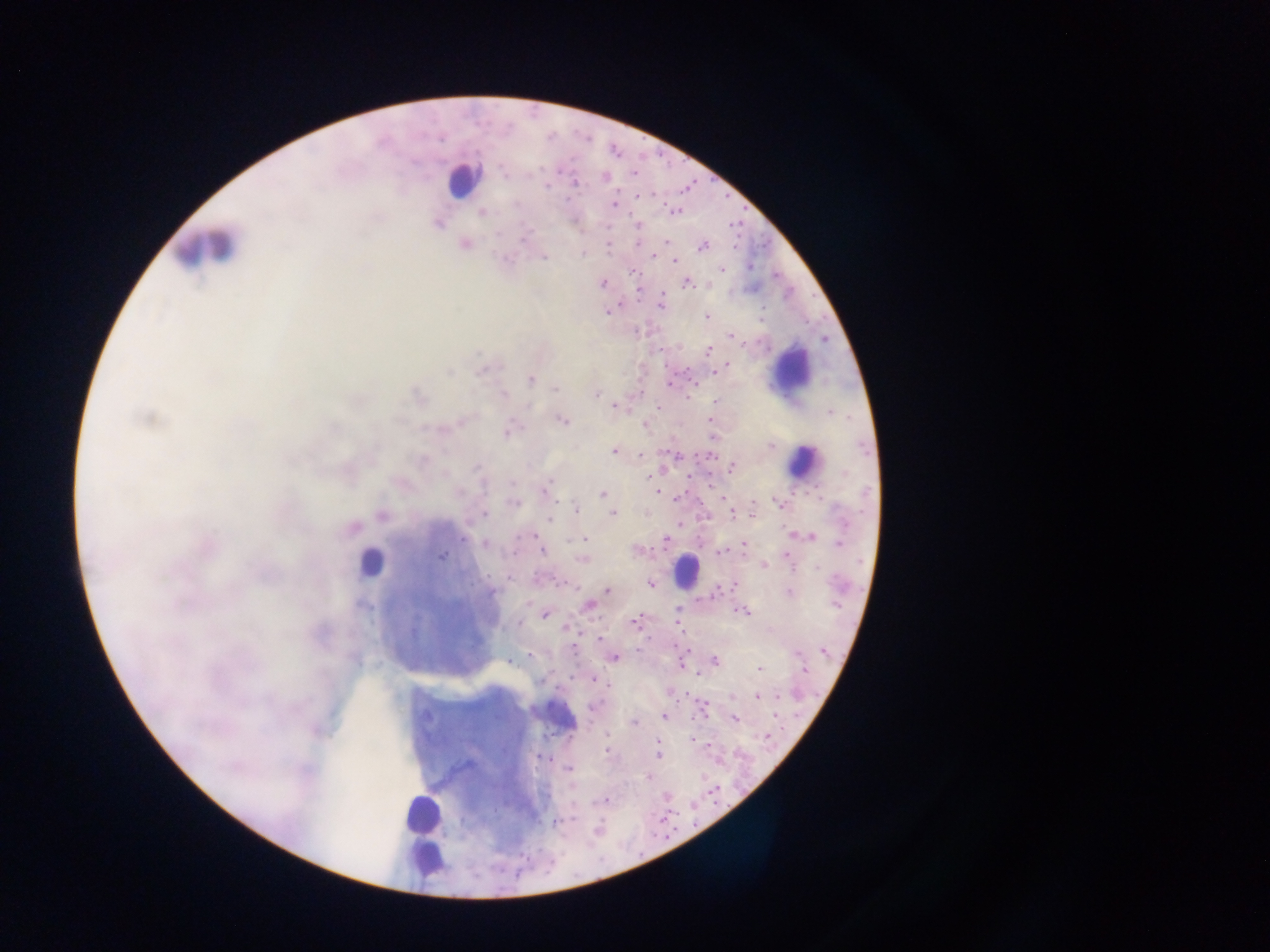

preparation = thick blood film
country = Ghana
image size = 1270×952 pixels
malaria parasite locations = approximate centers as {x, y} in pixels: {503, 174}, {529, 175}, {606, 177}, {575, 183}, {547, 186}, {638, 196}, {567, 200}, {614, 204}, {482, 212}, {438, 224}, {522, 239}, {638, 243}, {464, 244}, {702, 247}, {583, 253}, {653, 256}, {544, 257}, {674, 260}, {750, 266}, {721, 269}, {633, 272}, {603, 283}, {687, 283}, {662, 302}, {606, 312}, {707, 317}, {761, 319}, {732, 337}, {708, 349}, {480, 371}, {449, 372}, {715, 372}, {530, 379}, {670, 383}, {555, 388}, {596, 394}, {504, 395}, {689, 396}, {715, 402}, {615, 407}, {658, 407}, {830, 413}, {148, 418}, {562, 420}, {646, 426}, {507, 432}, {713, 436}, {771, 445}, {862, 448}, {613, 451}, {641, 455}, {678, 455}, {423, 460}, {476, 468}, {732, 469}, {514, 484}, {545, 491}, {655, 492}, {603, 493}, {514, 502}, {777, 502}, {753, 505}, {576, 508}, {732, 513}, {484, 514}, {612, 514}, {840, 514}, {381, 515}, {549, 519}, {351, 529}, {533, 536}, {812, 537}, {463, 539}, {584, 539}, {665, 541}, {485, 543}, {840, 544}, {744, 546}, {637, 550}, {543, 552}, {720, 554}, {441, 556}, {786, 556}, {581, 559}, {764, 565}, {791, 565}, {816, 568}, {510, 578}, {651, 583}, {734, 585}, {607, 590}, {790, 592}, {492, 593}, {835, 603}, {589, 606}, {677, 610}, {744, 611}, {544, 614}, {636, 621}, {520, 623}, {566, 627}, {600, 639}, {824, 651}, {798, 653}, {529, 655}, {614, 657}, {715, 660}, {509, 662}, {759, 669}, {804, 670}, {698, 676}, {594, 680}, {777, 695}, {734, 696}, {757, 697}, {594, 706}, {664, 716}, {735, 718}, {634, 722}, {607, 733}, {692, 739}, {658, 743}, {607, 751}, {658, 756}, {540, 758}, {568, 769}, {648, 777}, {604, 801}, {574, 819}, {555, 822}, {597, 828}
field of view = single
capture = mobile-phone photograph through a microscope
leukocyte locations = approximate centers as {x, y} in pixels: {461, 180}, {205, 249}, {791, 374}, {805, 461}, {369, 563}, {686, 570}, {556, 716}, {421, 814}, {424, 856}